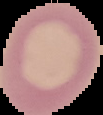 Result: no malaria parasites detected. From a thin blood smear. Cell region segmented out of the field of view; the surrounding area is masked to black. Image is 103×115 pixels.